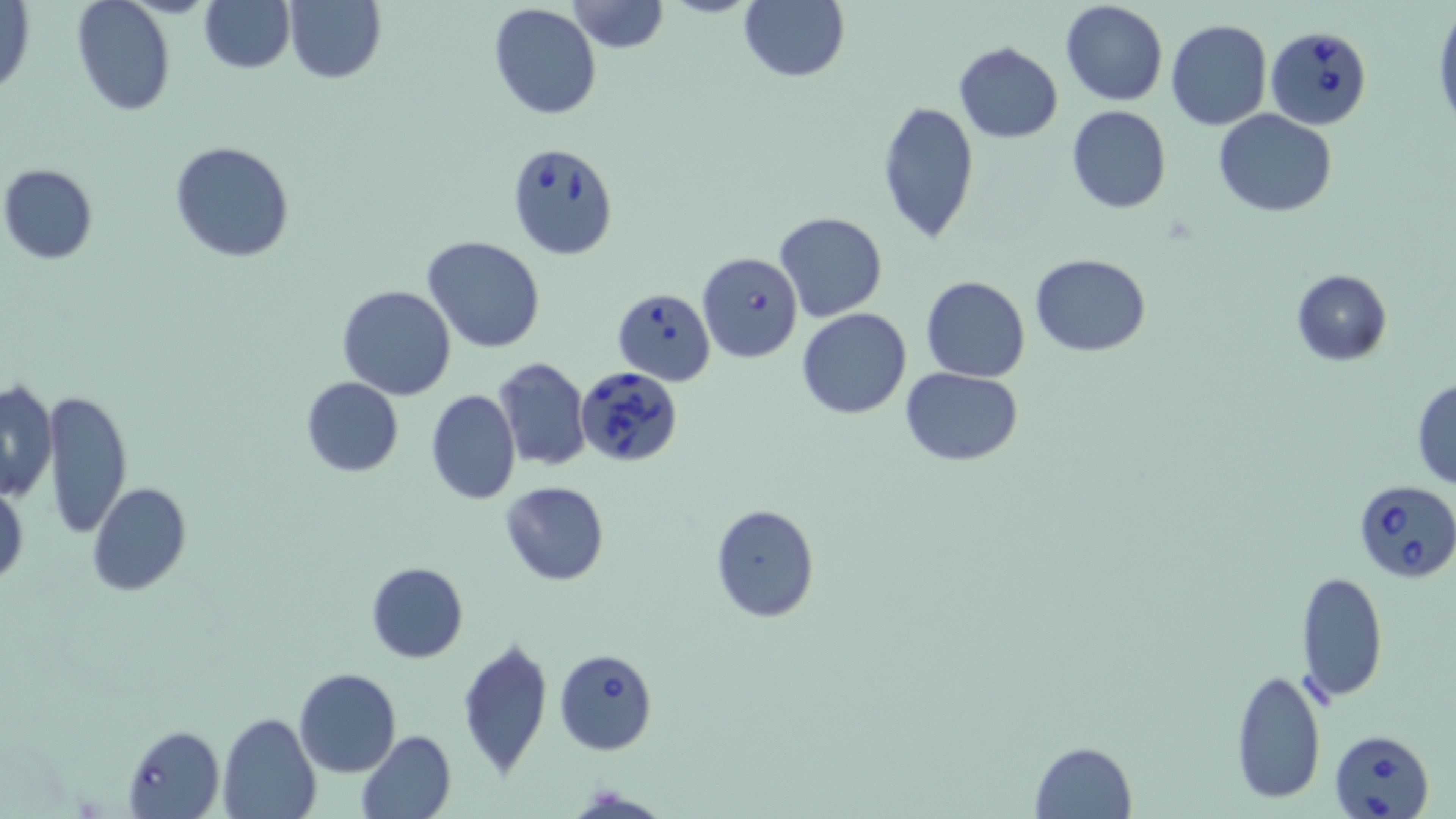

slide-level diagnosis = Babesia divergens
uninfected red blood cell locations = approximate bounding boxes as (x1,y1)-(x2,y2) corner pairs in pixels: (72,0)-(175,118), (198,0)-(294,73), (567,0)-(668,53), (739,0)-(849,82), (1059,0)-(1168,106), (284,1)-(385,84), (1,2)-(36,98), (487,3)-(602,120), (1433,8)-(1456,130), (1165,18)-(1272,130), (953,40)-(1062,143), (876,101)-(980,244), (1067,106)-(1171,215), (1214,109)-(1338,216), (171,140)-(294,262), (2,164)-(97,264), (775,213)-(888,323), (423,236)-(545,352), (1030,253)-(1152,356), (1291,268)-(1392,366), (920,275)-(1030,383), (337,285)-(456,400), (796,307)-(912,419), (494,359)-(593,471), (901,366)-(1024,466), (300,376)-(403,476), (1411,377)-(1456,488), (0,381)-(58,500), (44,388)-(132,539), (424,389)-(521,504), (0,481)-(27,589), (499,482)-(610,586), (87,483)-(190,597), (711,503)-(818,622), (365,562)-(468,664), (1297,572)-(1388,703), (457,637)-(553,777), (1231,665)-(1325,805), (294,668)-(401,777), (218,712)-(319,819), (357,730)-(457,819), (1029,741)-(1138,817)
image size = 1456×819 pixels
preparation = thin blood smear
stain = May-Grünwald-Giemsa
magnification = 1000x
modality = optical microscopy
Babesia divergens-infected red blood cell locations = approximate bounding boxes as (x1,y1)-(x2,y2) corner pairs in pixels: (1269,32)-(1372,132), (507,141)-(619,259), (698,251)-(804,363), (613,288)-(715,385), (576,366)-(682,467), (1353,479)-(1456,584), (555,649)-(657,755), (123,724)-(224,819), (1330,727)-(1435,819)
field of view = one of a larger specimen